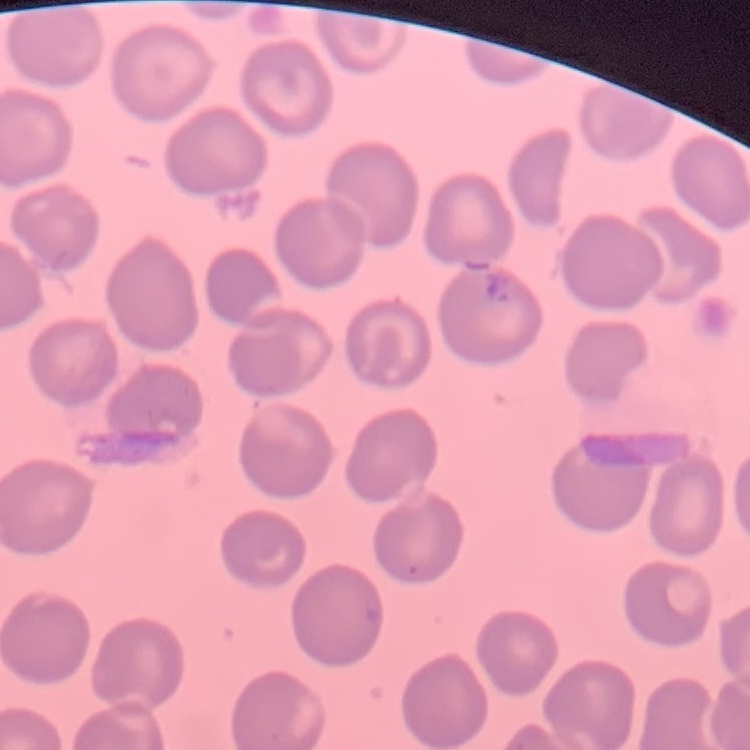

red blood cell morphology = no rouleaux formation
preparation = thin blood film
stain = Field's or Giemsa
image type = one tile cut from a larger photomicrograph